Report the malaria status of this cell.
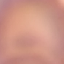
Uninfected.

stain: Giemsa
image_type: cell patch, automatically extracted from a larger field of view and resized to 64 × 64 pixels
capture: smartphone through the microscope eyepiece
preparation: thin blood smear